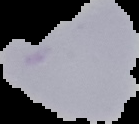

From a thin blood film. Result: no Plasmodium parasites detected. Image is 139×124 pixels. The area outside the segmented cell region is set to black.